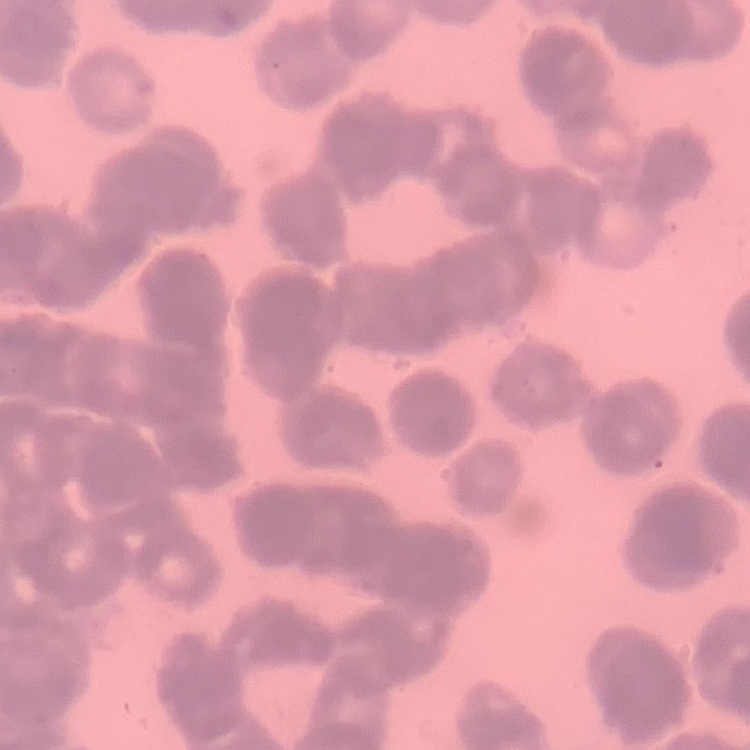
Summary:
  - Red blood cell morphology: rouleaux formation
  - Stain: Field's or Giemsa
  - Image type: square crop of a larger photomicrograph
  - Preparation: thin peripheral smear